Assess the morphology of the erythrocytes.
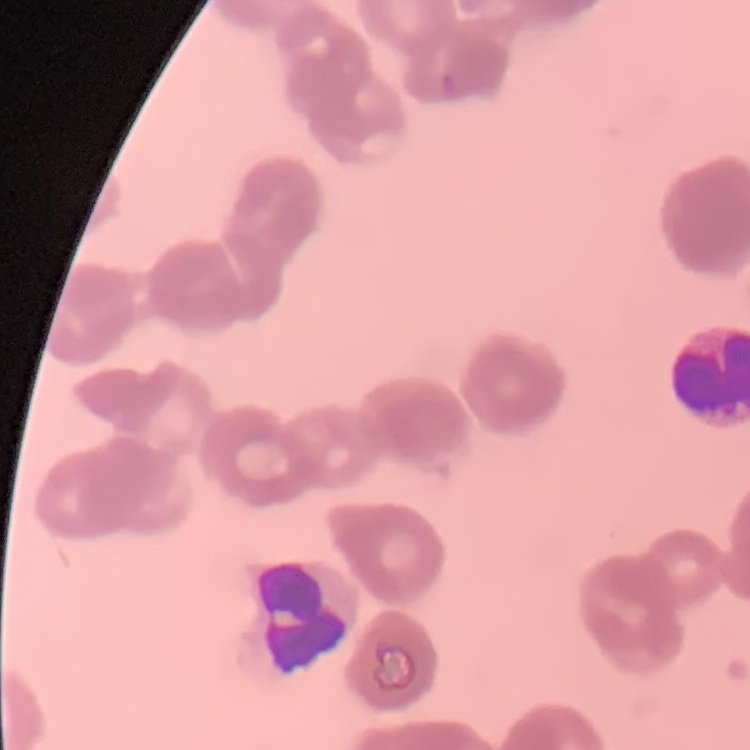
Rouleaux formation.

One tile cut from a larger photomicrograph. Field's or Giemsa stain. Thin blood film.